Assess the morphology of the erythrocytes.
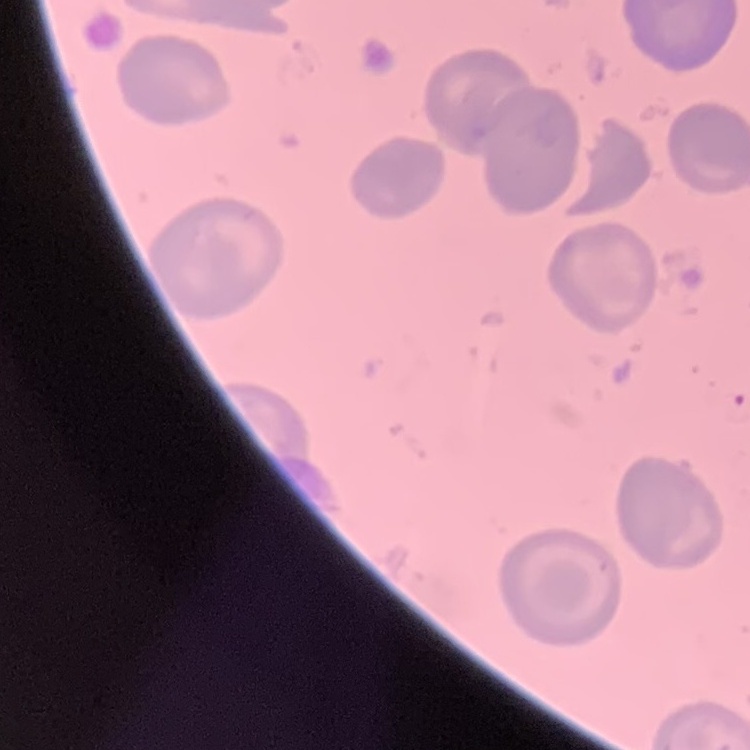

No rouleaux formation.

Thin blood smear. One tile cut from a larger photomicrograph. Field's or Giemsa stain.